Report the malaria status of this cell.
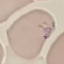
Parasitized.

Photographed with a smartphone camera at the microscope eyepiece. Automatically extracted cell patch, resized to 64 × 64 pixels. Giemsa stain. Thin smear of blood.